Assess the morphology of the red blood cells.
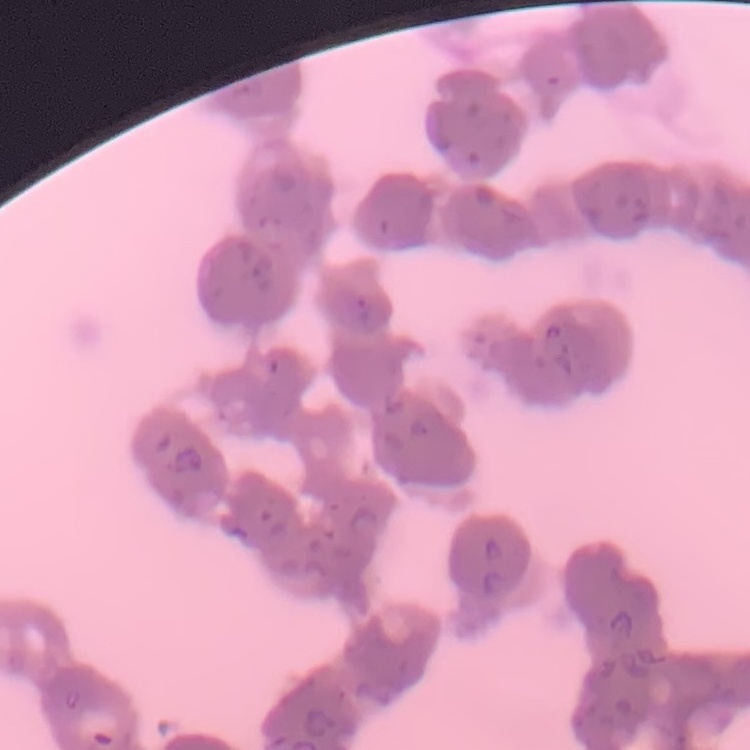

Rouleaux formation.

Summary:
  - Image type: one tile cut from a larger photomicrograph
  - Stain: Field's or Giemsa
  - Preparation: thin blood smear